Give the position of every malaria parasite.
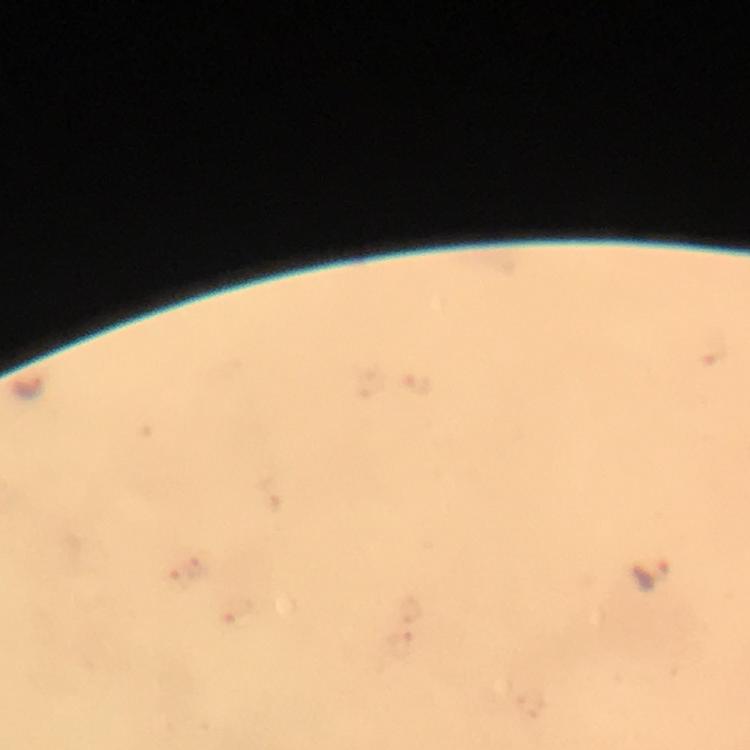
Approximate centers as [x, y] in pixels.
Malaria parasites: [653, 573].

Summary:
  - Cropped from: a single field of view
  - Immersion oil: applied
  - Capture: smartphone mounted on the microscope
  - Magnification: 100x
  - Preparation: thick smear
  - Context: from a malaria diagnostic workup
  - Stain: Giemsa
  - Image size: 750×750 pixels